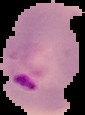 Image is 85×115 pixels. Cell region segmented out of the field of view; the surrounding area is masked to black. Result: malaria parasites identified. From a thin blood smear.